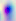
Summary:
  - Identification: Toxoplasma gondii
  - Magnification: 400x
  - Modality: photomicrograph